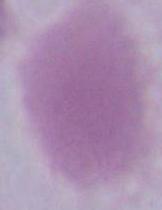

identification = red blood cell
modality = photomicrograph
magnification = 1000x